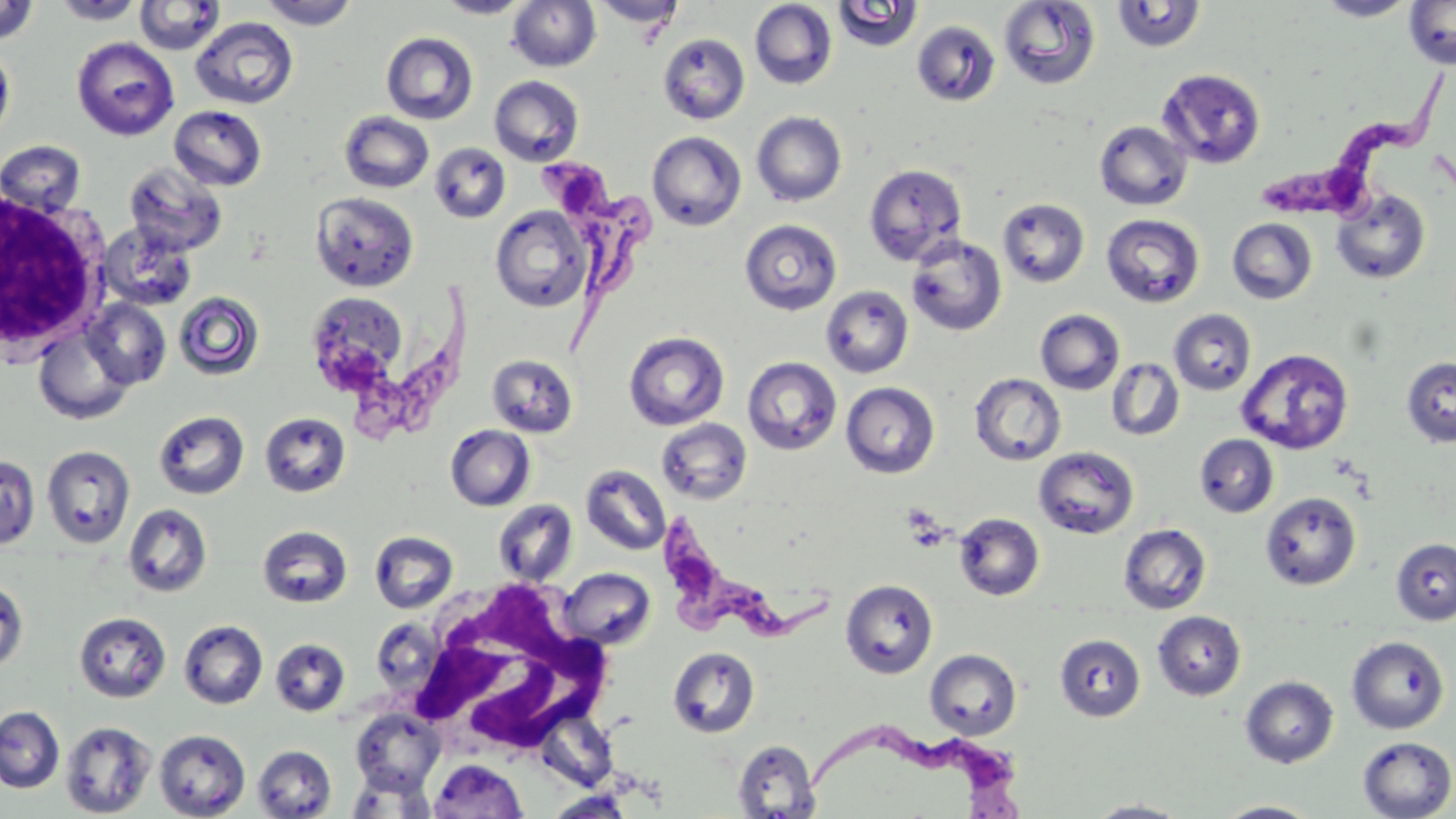
Summary:
  - Coordinate format: approximate bounding boxes as named x1/y1/x2/y2 corners in pixels
  - White blood cell locations: (x1=0, y1=185, x2=109, y2=358), (x1=398, y1=576, x2=622, y2=762)
  - Uninfected red blood cell locations: (x1=51, y1=0, x2=146, y2=25), (x1=134, y1=0, x2=225, y2=55), (x1=258, y1=0, x2=361, y2=29), (x1=436, y1=0, x2=533, y2=18), (x1=507, y1=0, x2=601, y2=72), (x1=590, y1=0, x2=685, y2=30), (x1=999, y1=0, x2=1101, y2=90), (x1=1314, y1=0, x2=1419, y2=21), (x1=0, y1=1, x2=38, y2=44), (x1=749, y1=1, x2=837, y2=89), (x1=1111, y1=1, x2=1207, y2=53), (x1=832, y1=2, x2=924, y2=53), (x1=1403, y1=2, x2=1456, y2=69), (x1=190, y1=17, x2=299, y2=109), (x1=912, y1=20, x2=1001, y2=106), (x1=381, y1=31, x2=479, y2=125), (x1=658, y1=33, x2=749, y2=125), (x1=71, y1=37, x2=179, y2=141), (x1=0, y1=42, x2=15, y2=147), (x1=1157, y1=68, x2=1266, y2=168), (x1=489, y1=75, x2=584, y2=166), (x1=169, y1=106, x2=268, y2=191), (x1=339, y1=111, x2=434, y2=193), (x1=751, y1=111, x2=847, y2=206), (x1=1095, y1=121, x2=1192, y2=211), (x1=647, y1=131, x2=746, y2=231), (x1=0, y1=140, x2=88, y2=218), (x1=429, y1=143, x2=511, y2=222), (x1=123, y1=162, x2=228, y2=257), (x1=864, y1=163, x2=967, y2=266), (x1=1330, y1=188, x2=1431, y2=285), (x1=310, y1=191, x2=419, y2=293), (x1=998, y1=198, x2=1090, y2=288), (x1=490, y1=206, x2=592, y2=313), (x1=1101, y1=214, x2=1205, y2=308), (x1=1227, y1=218, x2=1317, y2=304), (x1=739, y1=219, x2=842, y2=316), (x1=98, y1=223, x2=198, y2=312), (x1=906, y1=234, x2=1007, y2=336), (x1=821, y1=286, x2=913, y2=378), (x1=305, y1=291, x2=412, y2=396), (x1=174, y1=292, x2=264, y2=380), (x1=83, y1=298, x2=171, y2=390), (x1=1035, y1=309, x2=1125, y2=395), (x1=1169, y1=309, x2=1256, y2=395), (x1=33, y1=324, x2=134, y2=424), (x1=624, y1=331, x2=729, y2=431), (x1=1236, y1=348, x2=1355, y2=455), (x1=486, y1=354, x2=579, y2=438), (x1=1401, y1=355, x2=1456, y2=448), (x1=742, y1=357, x2=842, y2=455), (x1=1106, y1=358, x2=1185, y2=441), (x1=969, y1=373, x2=1066, y2=466), (x1=840, y1=382, x2=940, y2=478), (x1=153, y1=410, x2=249, y2=500), (x1=259, y1=412, x2=350, y2=498), (x1=655, y1=419, x2=752, y2=505), (x1=445, y1=425, x2=535, y2=511), (x1=1194, y1=434, x2=1279, y2=517), (x1=41, y1=445, x2=136, y2=548), (x1=1033, y1=446, x2=1139, y2=539), (x1=0, y1=455, x2=40, y2=550), (x1=580, y1=464, x2=671, y2=555), (x1=1260, y1=492, x2=1361, y2=590), (x1=493, y1=499, x2=578, y2=586), (x1=122, y1=504, x2=213, y2=598), (x1=954, y1=512, x2=1045, y2=601), (x1=1118, y1=524, x2=1212, y2=615), (x1=257, y1=525, x2=353, y2=608), (x1=369, y1=530, x2=458, y2=613), (x1=1391, y1=537, x2=1456, y2=625), (x1=559, y1=568, x2=656, y2=650), (x1=0, y1=579, x2=28, y2=673), (x1=840, y1=579, x2=938, y2=678), (x1=74, y1=611, x2=171, y2=703), (x1=1152, y1=611, x2=1246, y2=700), (x1=179, y1=619, x2=268, y2=709), (x1=1054, y1=633, x2=1146, y2=721), (x1=1346, y1=636, x2=1449, y2=734), (x1=270, y1=638, x2=351, y2=716), (x1=668, y1=646, x2=760, y2=738), (x1=925, y1=648, x2=1022, y2=740), (x1=1239, y1=676, x2=1339, y2=768), (x1=0, y1=706, x2=64, y2=793), (x1=350, y1=708, x2=444, y2=795), (x1=534, y1=709, x2=619, y2=790), (x1=60, y1=721, x2=157, y2=818), (x1=154, y1=729, x2=251, y2=818), (x1=1357, y1=735, x2=1455, y2=819), (x1=732, y1=739, x2=822, y2=818), (x1=252, y1=744, x2=336, y2=818), (x1=429, y1=759, x2=528, y2=818), (x1=345, y1=769, x2=437, y2=818), (x1=1083, y1=799, x2=1193, y2=818), (x1=1213, y1=800, x2=1323, y2=818)
  - Trypanosoma brucei locations: (x1=1251, y1=74, x2=1447, y2=222), (x1=543, y1=149, x2=654, y2=360), (x1=331, y1=281, x2=479, y2=434), (x1=657, y1=519, x2=838, y2=648), (x1=808, y1=725, x2=1023, y2=819)
  - Slide-level diagnosis: Trypanosoma brucei
  - Field of view: one of a larger specimen
  - Modality: light microscopy
  - Preparation: thin blood smear
  - Image size: 1456×819 pixels
  - Magnification: 1000x
  - Stain: May-Grünwald-Giemsa